Locate every Plasmodium parasite and every leukocyte.
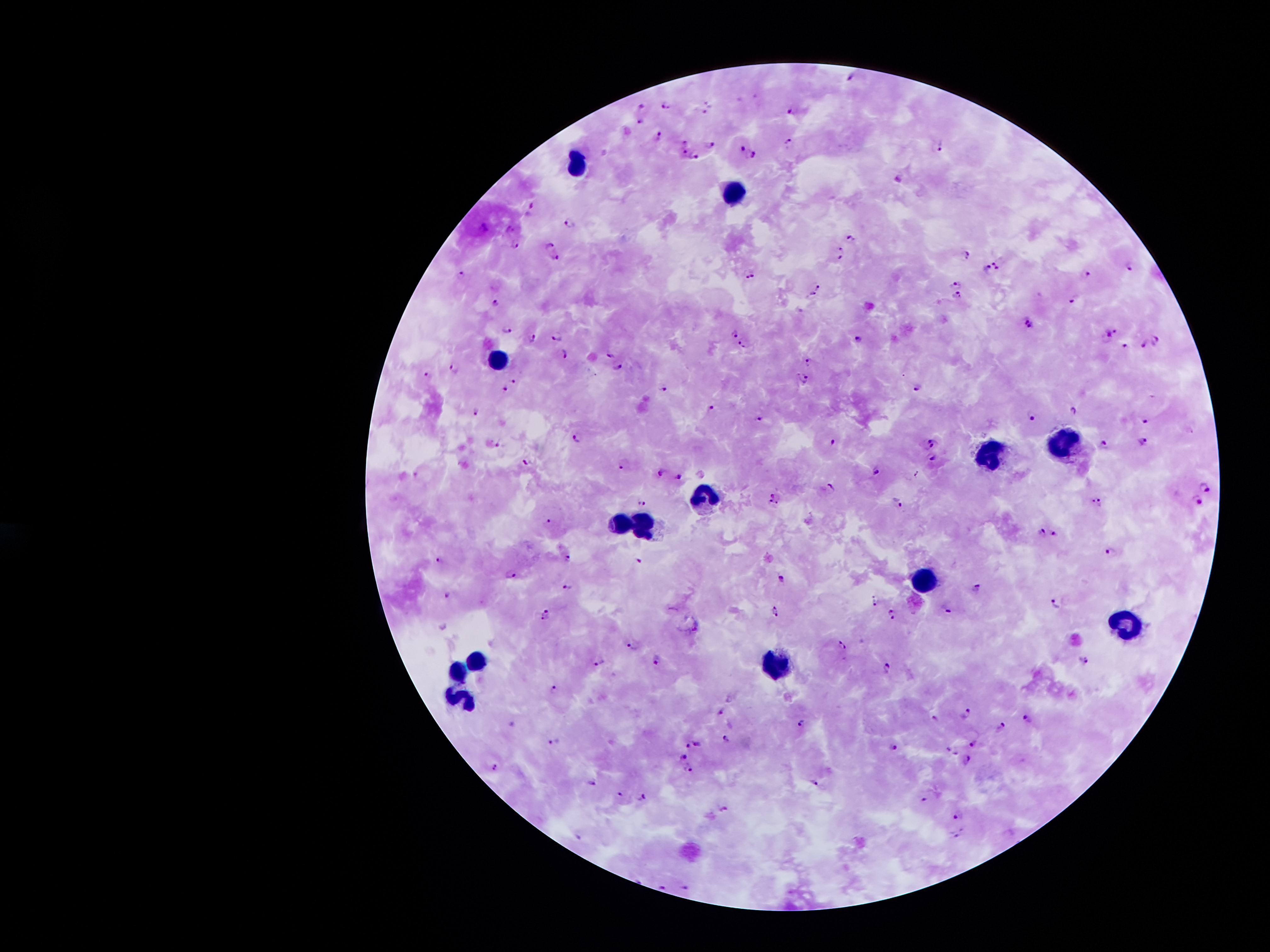

Approximate centers as (x, y) in pixels.
Plasmodium parasites: (851, 75), (665, 105), (640, 106), (704, 111), (789, 111), (641, 121), (657, 138), (684, 141), (788, 142), (711, 145), (743, 146), (941, 146), (684, 150), (753, 154), (694, 156), (899, 179), (570, 224), (852, 239), (547, 245), (516, 247), (841, 250), (967, 255), (554, 258), (840, 259), (994, 263), (1131, 267), (985, 269), (997, 269), (754, 272), (464, 274), (1088, 274), (743, 278), (956, 285), (819, 288), (812, 294), (956, 296), (1074, 299), (495, 303), (1025, 318), (1032, 327), (507, 329), (1115, 329), (736, 333), (1108, 333), (532, 337), (557, 337), (859, 340), (1156, 341), (743, 344), (1144, 344), (1126, 346), (565, 353), (610, 356), (810, 361), (454, 367), (619, 367), (428, 373), (804, 378), (514, 381), (505, 388), (919, 388), (664, 389), (1074, 410), (711, 411), (477, 412), (1032, 416), (759, 418), (1145, 421), (576, 437), (934, 437), (833, 441), (1143, 441), (1104, 445), (929, 447), (933, 458), (529, 461), (622, 465), (877, 470), (661, 472), (916, 473), (680, 475), (832, 488), (1205, 488), (774, 494), (1198, 499), (899, 501), (1098, 501), (645, 503), (773, 506), (548, 521), (1042, 532), (1054, 533), (1112, 550), (569, 557), (639, 561), (441, 562), (511, 574), (782, 578), (568, 588), (976, 588), (448, 594), (876, 600), (1056, 602), (946, 608), (892, 610), (776, 612), (547, 615), (894, 618), (841, 644), (632, 647), (1085, 660), (600, 662), (657, 662), (886, 668), (555, 688), (721, 710), (967, 714), (934, 716), (1027, 718), (801, 723), (1000, 726), (726, 738), (553, 741), (698, 743), (972, 743), (688, 745), (895, 747), (947, 748), (956, 753), (683, 756), (967, 760), (494, 767), (690, 768), (815, 782), (591, 784), (621, 794), (642, 796), (923, 797), (724, 809), (957, 815), (959, 836), (686, 886), (663, 887).
Leukocytes: (576, 167), (733, 193), (502, 362), (1066, 444), (989, 454), (709, 495), (622, 524), (649, 525), (927, 579), (1127, 622), (1129, 626), (479, 660), (775, 663), (459, 674), (462, 696).

One field from this slide. 100x magnification. Thick blood film. Image is 1270×952 pixels. Patient malaria status: infected with Plasmodium falciparum. Photographed through the microscope eyepiece with a smartphone camera. Giemsa stain.